Identify the parasite.
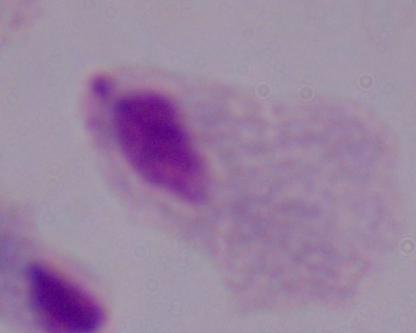
This is a trichomonad.

magnification = 1000x
modality = photomicrograph